Comment on the morphology of the red blood cells.
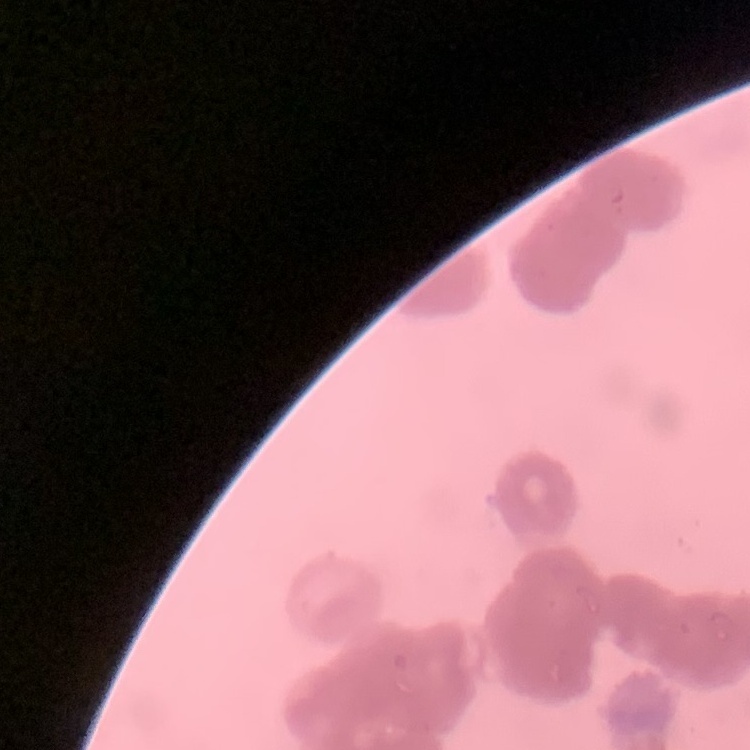
Rouleaux formation.

Summary:
  - Preparation: thin peripheral smear
  - Image type: square crop of a larger photomicrograph
  - Stain: Field's or Giemsa